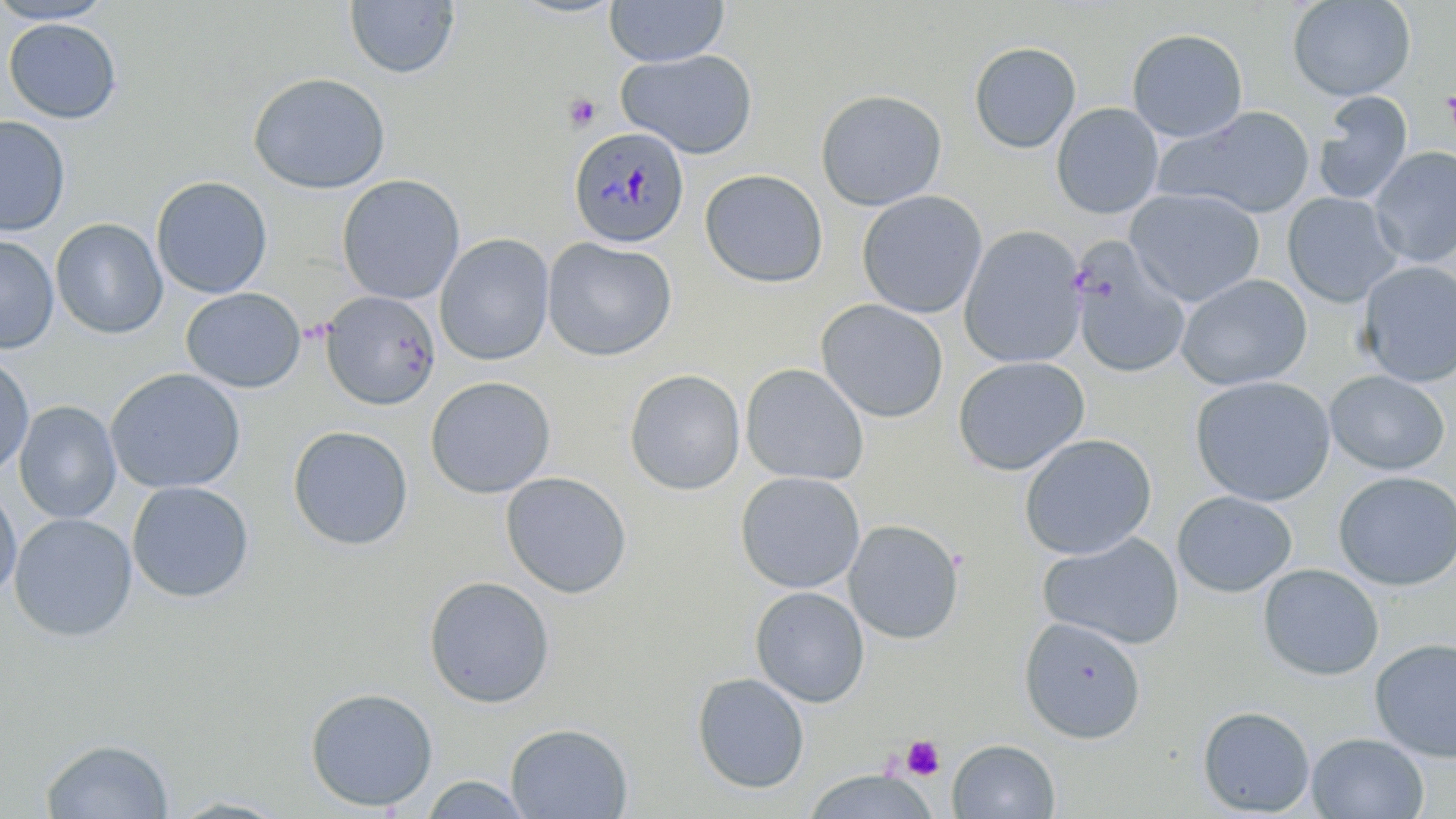
{
  "slide_level_diagnosis": "Plasmodium malariae",
  "modality": "optical microscopy",
  "preparation": "thin blood film",
  "platelet_locations": "approximate bounding boxes as [x1, y1, x2, y2] in pixels: [1441, 83, 1456, 146], [564, 94, 601, 131], [901, 735, 945, 780]",
  "plasmodium_malariae_infected_red_blood_cell_locations": "approximate bounding boxes as [x1, y1, x2, y2] in pixels: [570, 126, 692, 255]",
  "field_of_view": "one of a larger specimen",
  "stain": "May-Grünwald-Giemsa",
  "uninfected_red_blood_cell_locations": "approximate bounding boxes as [x1, y1, x2, y2] in pixels: [0, 0, 116, 24], [605, 0, 729, 67], [1287, 0, 1417, 101], [344, 1, 459, 79], [2, 18, 122, 123], [1126, 27, 1248, 142], [968, 41, 1082, 154], [616, 49, 758, 159], [248, 72, 391, 194], [815, 89, 947, 211], [1312, 90, 1414, 205], [1050, 102, 1164, 219], [1157, 105, 1317, 218], [0, 115, 71, 237], [1370, 146, 1456, 267], [700, 169, 828, 288], [337, 174, 465, 305], [151, 176, 273, 299], [1125, 188, 1265, 306], [857, 190, 988, 319], [1282, 192, 1404, 307], [50, 218, 168, 340], [958, 225, 1087, 369], [435, 233, 554, 366], [0, 234, 59, 354], [541, 237, 678, 362], [1068, 237, 1192, 380], [1356, 260, 1456, 387], [1176, 274, 1312, 391], [181, 287, 307, 393], [319, 290, 441, 411], [815, 298, 949, 423], [0, 351, 35, 480], [952, 356, 1090, 476], [740, 363, 869, 485], [105, 368, 246, 494], [625, 369, 746, 495], [1325, 369, 1450, 475], [1189, 375, 1336, 506], [425, 376, 556, 499], [13, 400, 122, 524], [287, 425, 414, 551], [1019, 433, 1157, 560], [735, 471, 866, 594], [1333, 471, 1456, 591], [500, 472, 632, 599], [126, 480, 255, 603], [0, 486, 22, 600], [1172, 491, 1298, 597], [9, 512, 138, 642], [843, 519, 964, 645], [1037, 533, 1185, 650], [1258, 564, 1384, 681], [422, 575, 556, 709], [750, 586, 869, 707], [1019, 616, 1146, 744], [1369, 637, 1456, 763], [692, 672, 810, 794], [304, 686, 438, 812], [1197, 705, 1315, 817], [505, 723, 633, 818], [1306, 732, 1430, 818], [40, 738, 175, 818], [947, 738, 1060, 818], [801, 769, 940, 819], [420, 775, 532, 818], [164, 794, 295, 818]",
  "magnification": "1000x",
  "image_size": "1456×819 pixels"
}